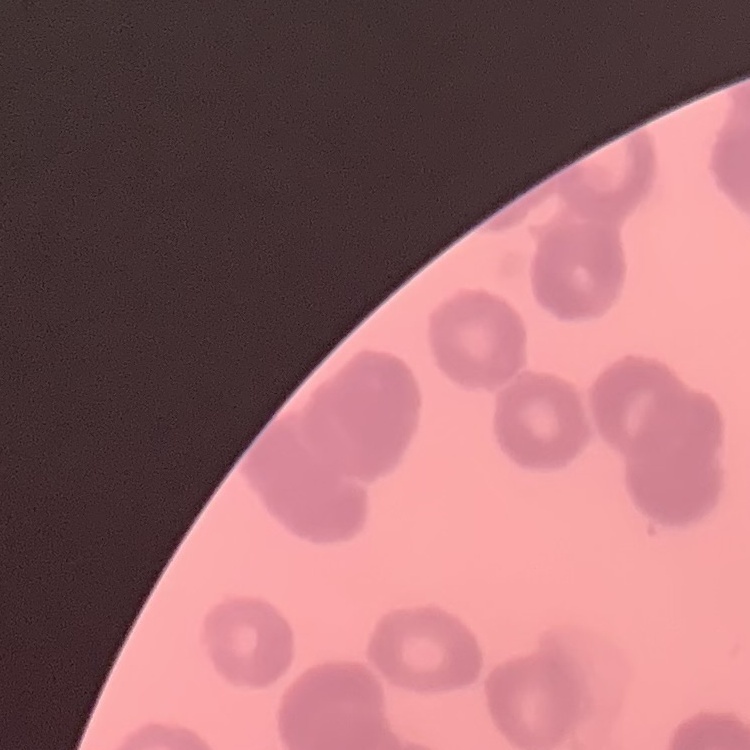

Summary:
  - Red blood cell morphology: rouleaux formation
  - Preparation: thin blood film
  - Stain: Field's or Giemsa
  - Image type: square crop of a larger photomicrograph